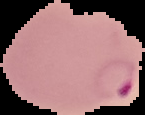
preparation = thin blood smear
result = Plasmodium parasites detected
image size = 145×115 pixels
image type = segmented cell region on a black background